State which parasite is depicted.
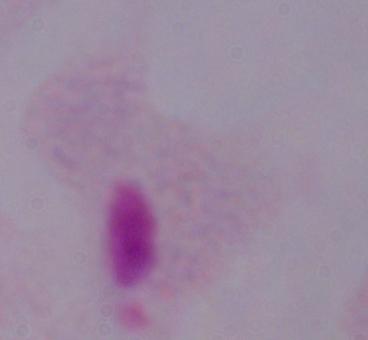

This is a trichomonad.

{
  "magnification": "1000x",
  "modality": "photomicrograph"
}